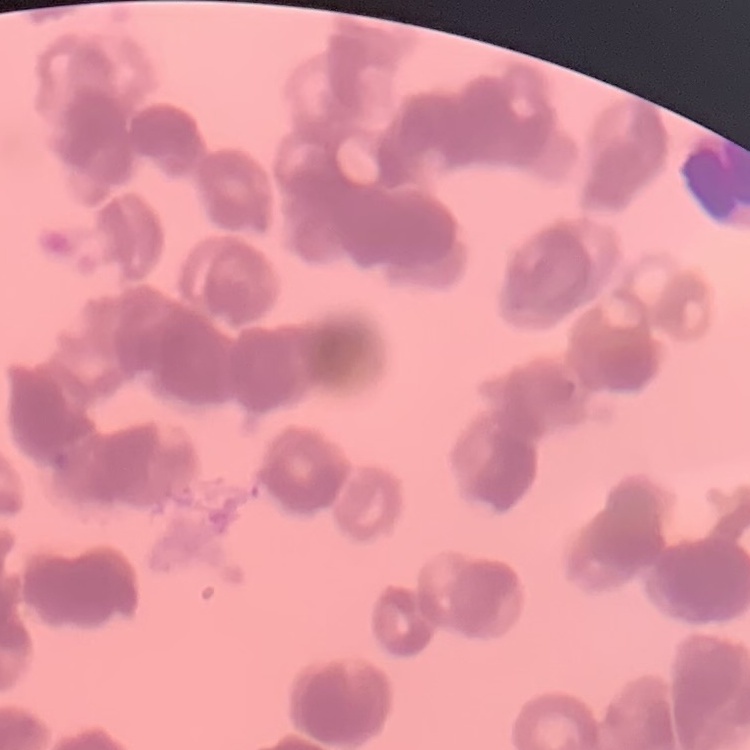

red_blood_cell_morphology: rouleaux formation
stain: Field's or Giemsa
image_type: one tile cut from a larger photomicrograph
preparation: thin blood smear